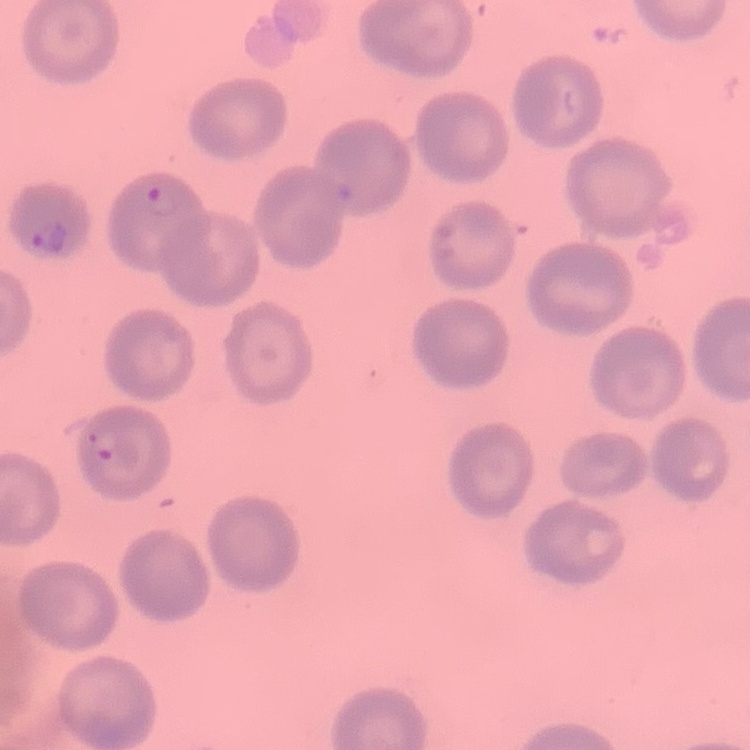

Summary:
  - Red blood cell morphology: no rouleaux formation
  - Preparation: thin blood smear
  - Stain: Field's or Giemsa
  - Image type: one tile cut from a larger photomicrograph